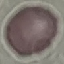
Summary:
  - Malaria status: uninfected
  - Capture: smartphone camera at the microscope eyepiece
  - Stain: Giemsa
  - Preparation: thin smear
  - Image type: automatically extracted cell patch, resized to 64 × 64 pixels